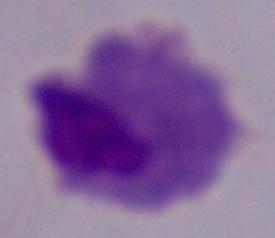

1000x magnification. A trichomonad is shown. Micrograph.